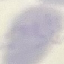
malaria status = uninfected
capture = smartphone camera at the microscope eyepiece
image type = cell patch, automatically extracted from a larger field of view and resized to 64 × 64 pixels
stain = Giemsa
preparation = thin blood film